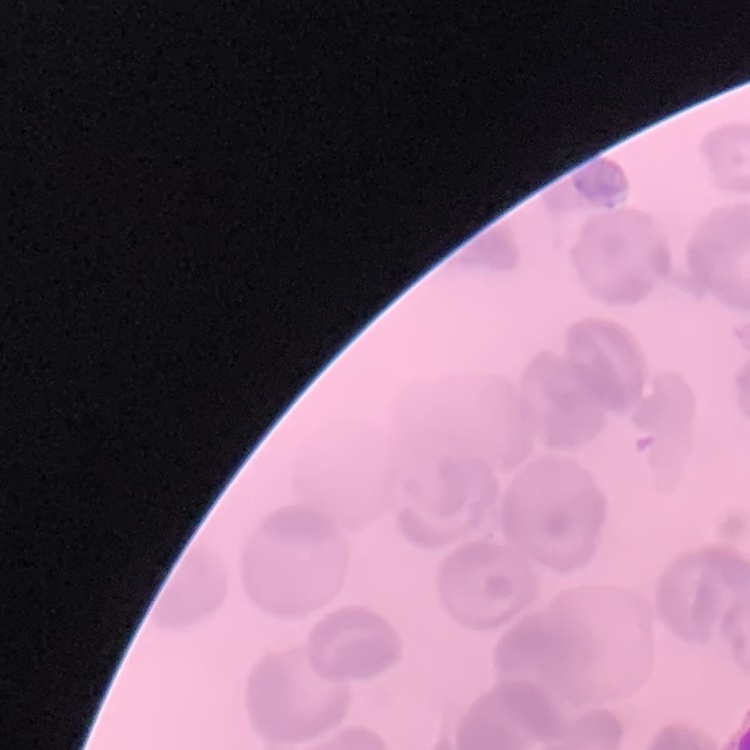
red_blood_cell_morphology: no rouleaux formation
preparation: thin peripheral smear
image_type: one tile cut from a larger photomicrograph
stain: Field's or Giemsa